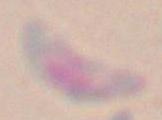

Micrograph. Toxoplasma gondii is seen. Captured at 1000x magnification.